Assess the background quality.
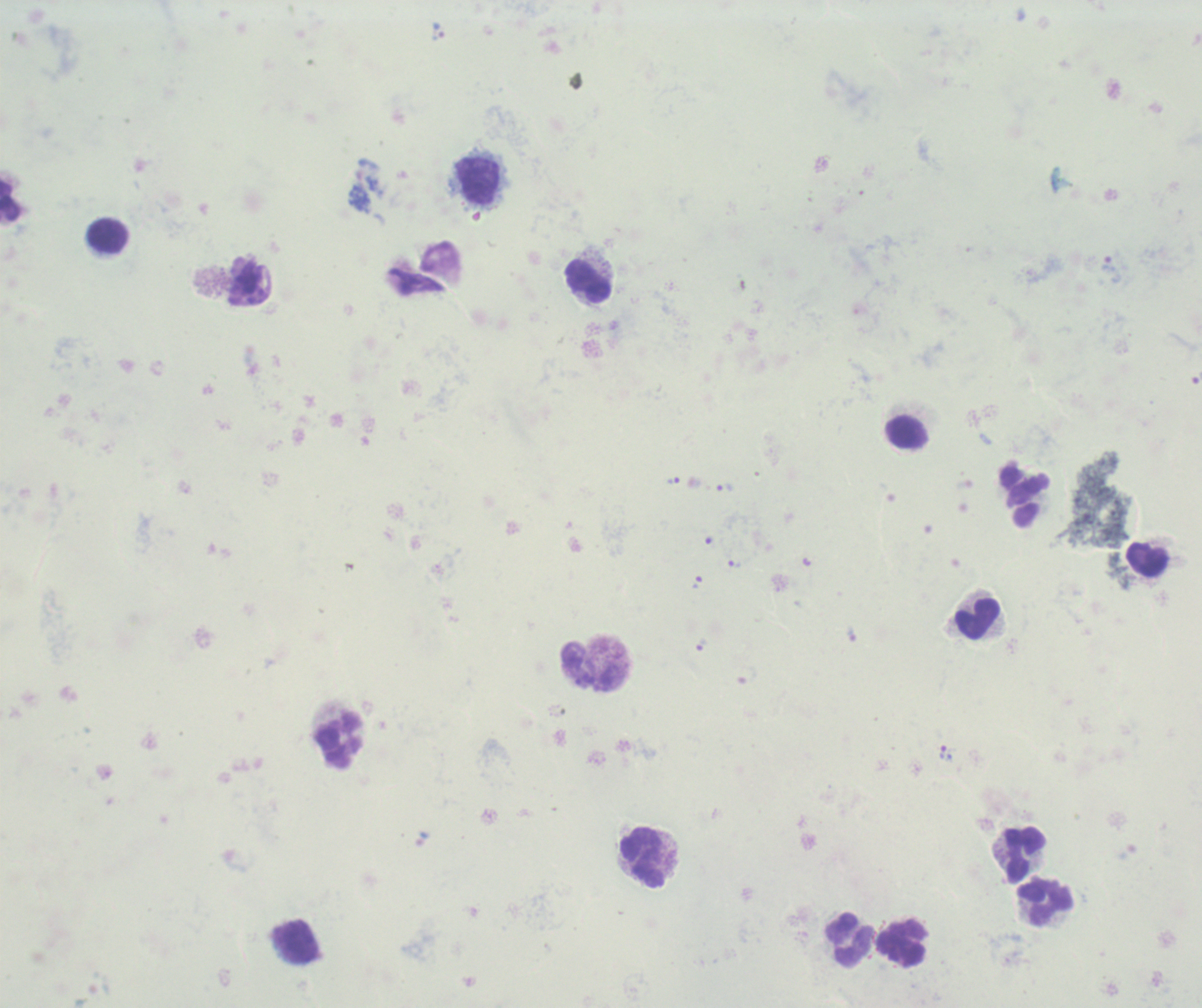
Unsatisfactory.

Approximate centers as {x, y} in pixels. Leukocyte locations: {478, 181}, {107, 237}, {589, 281}, {907, 432}, {1025, 496}, {1147, 559}, {977, 619}, {593, 666}, {338, 739}, {1025, 853}, {643, 857}, {1046, 902}, {849, 939}, {295, 942}, {901, 944}. Trophozoite locations: {437, 32}, {1111, 269}, {673, 481}, {725, 489}, {734, 564}, {697, 583}, {851, 636}, {701, 645}, {943, 752}. Single field of view. Result: Plasmodium parasites detected. Thick smear of blood. Image is 1202×1008 pixels. 100x magnification. Previously used in an actual diagnosis. Romanowsky-stained preparation.